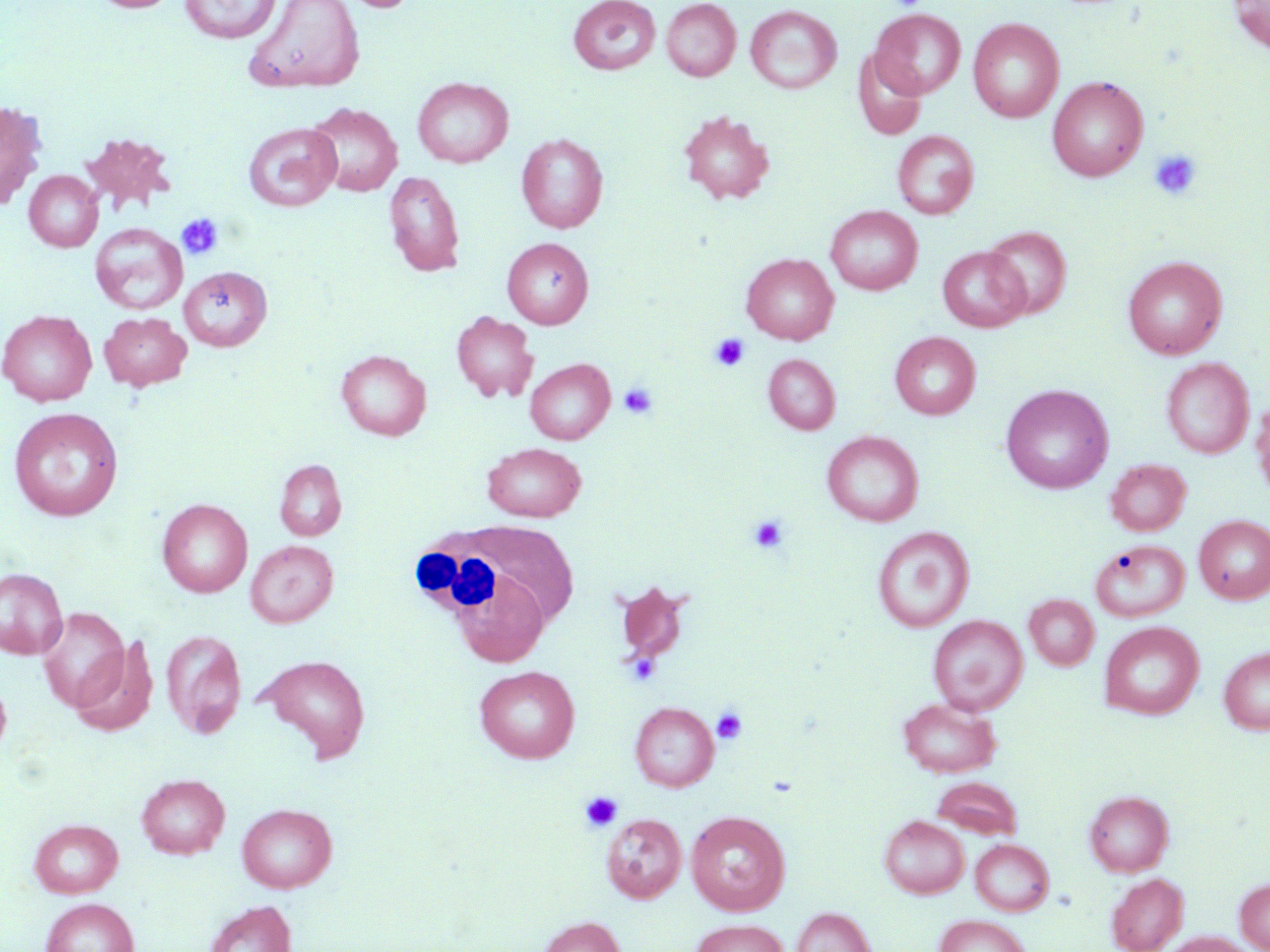

Approximate bounding boxes as (x1,y1)-(x2,y2) corner pairs in pixels. Platelet locations: (1149,149)-(1202,201), (176,213)-(225,260), (710,333)-(750,372), (618,381)-(658,420), (748,514)-(790,553), (711,707)-(748,744), (580,791)-(622,831). White blood cell locations: (411,521)-(579,629). Uninfected red blood cell locations: (90,0)-(181,13), (179,0)-(282,44), (243,0)-(365,94), (334,0)-(421,13), (661,0)-(741,81), (1229,0)-(1270,53), (568,1)-(662,75), (745,5)-(841,94), (871,8)-(966,98), (968,18)-(1064,123), (852,48)-(928,140), (412,76)-(513,167), (1047,76)-(1148,181), (0,100)-(48,210), (307,103)-(402,196), (677,111)-(775,205), (243,122)-(342,212), (79,131)-(176,215), (892,131)-(979,218), (516,133)-(608,233), (24,170)-(103,252), (384,170)-(466,276), (825,206)-(923,295), (89,223)-(188,316), (982,225)-(1072,319), (502,237)-(594,328), (937,246)-(1029,332), (742,254)-(838,344), (1122,255)-(1227,359), (179,266)-(271,351), (0,310)-(97,406), (451,310)-(539,403), (99,312)-(192,391), (890,332)-(981,420), (336,349)-(431,440), (764,354)-(840,434), (1161,357)-(1254,459), (525,358)-(614,445), (1000,384)-(1113,494), (1251,398)-(1270,503), (8,407)-(123,521), (822,430)-(923,527), (483,442)-(587,521), (274,459)-(347,541), (1105,459)-(1191,536), (157,499)-(252,597), (1194,515)-(1270,604), (872,526)-(975,632), (246,540)-(338,628), (1091,540)-(1190,623), (0,567)-(68,660), (452,569)-(550,667), (613,580)-(691,665), (1024,594)-(1099,670), (37,607)-(129,710), (928,615)-(1028,714), (1099,621)-(1205,720), (161,629)-(246,738), (70,636)-(159,737), (1219,646)-(1270,734), (255,654)-(371,762), (475,665)-(580,763), (0,678)-(12,759), (897,697)-(1001,778), (630,702)-(719,791), (136,773)-(230,859), (931,775)-(1023,840), (1084,790)-(1174,876), (236,802)-(337,892), (685,810)-(791,915), (601,814)-(686,902), (879,815)-(970,898), (30,819)-(123,898), (970,838)-(1054,915), (1106,873)-(1187,952), (1235,878)-(1270,951), (41,898)-(139,952), (204,900)-(296,952), (792,907)-(875,952), (934,914)-(1033,952), (536,916)-(626,952), (690,919)-(791,952), (1163,932)-(1257,952). Slide-level diagnosis: no evidence of blood parasites. Thin blood film. May-Grünwald-Giemsa stain. Light microscopy. 1000x magnification. Image is 1270×952 pixels. Single field of view.